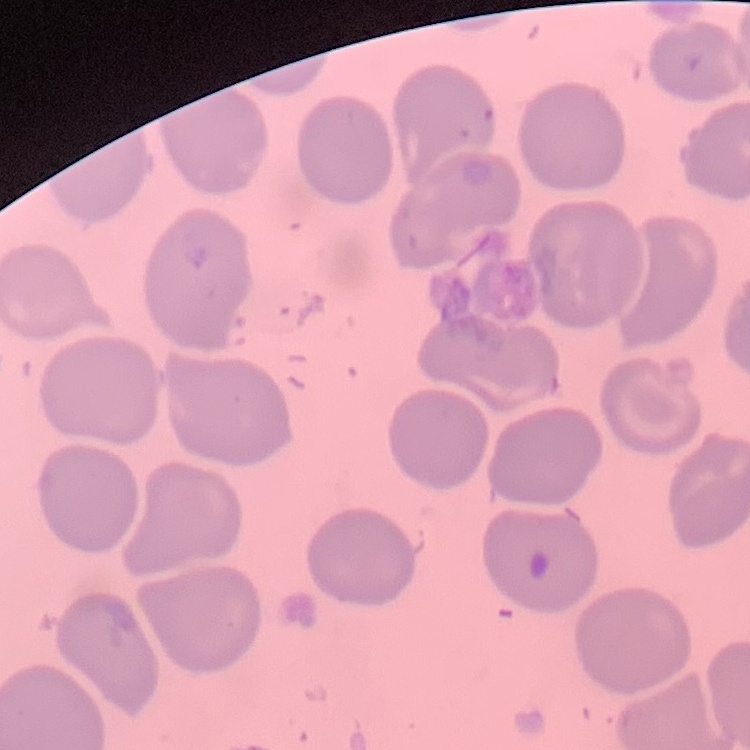

Summary:
  - Erythrocyte morphology: no rouleaux formation
  - Image type: one tile cut from a larger photomicrograph
  - Preparation: thin blood smear
  - Stain: Field's or Giemsa